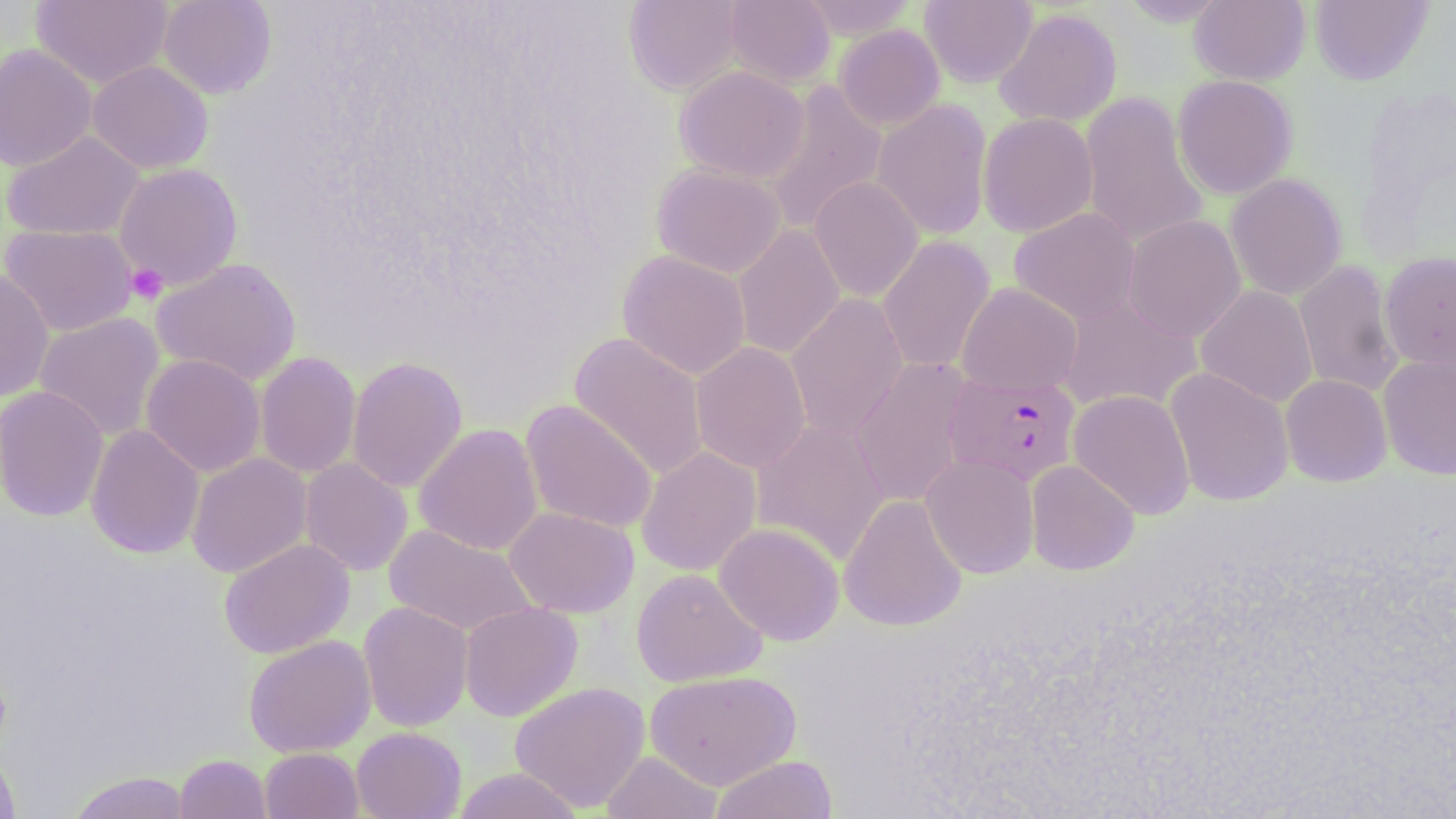

Summary:
  - Coordinate format: approximate bounding boxes as (x1, y1, x2, y2) in pixels
  - Plasmodium falciparum-infected red blood cell locations: (944, 371, 1081, 487)
  - Platelet locations: (126, 263, 168, 305)
  - Uninfected red blood cell locations: (31, 0, 173, 89), (157, 0, 277, 99), (624, 0, 745, 95), (723, 0, 836, 88), (797, 0, 919, 39), (920, 0, 1037, 88), (1119, 0, 1231, 26), (1190, 0, 1310, 85), (1310, 0, 1432, 85), (994, 7, 1122, 128), (833, 24, 945, 131), (0, 43, 98, 171), (87, 60, 213, 174), (674, 65, 810, 183), (1172, 74, 1297, 199), (761, 81, 888, 235), (1079, 92, 1209, 250), (872, 99, 992, 241), (978, 112, 1098, 238), (2, 130, 144, 241), (114, 162, 244, 290), (651, 163, 787, 278), (1226, 173, 1346, 300), (808, 176, 924, 303), (1009, 207, 1140, 324), (1123, 214, 1246, 342), (0, 224, 139, 336), (732, 225, 845, 359), (877, 235, 996, 374), (616, 250, 752, 380), (1379, 251, 1456, 371), (151, 258, 302, 386), (1294, 260, 1404, 398), (0, 268, 54, 401), (956, 283, 1083, 396), (1196, 285, 1318, 408), (786, 292, 909, 442), (1055, 292, 1203, 414), (34, 312, 166, 442), (569, 332, 709, 481), (691, 342, 811, 473), (255, 351, 361, 479), (141, 354, 266, 477), (1378, 354, 1456, 480), (346, 356, 468, 493), (850, 358, 974, 507), (1165, 367, 1294, 507), (1281, 374, 1392, 486), (0, 385, 110, 522), (1069, 389, 1195, 519), (520, 400, 658, 534), (751, 419, 890, 566), (414, 423, 543, 556), (85, 424, 205, 559), (636, 446, 762, 576), (187, 453, 312, 578), (920, 453, 1040, 579), (300, 457, 413, 576), (1026, 460, 1139, 575), (839, 494, 967, 632), (504, 506, 639, 618), (714, 522, 844, 645), (384, 524, 538, 637), (219, 538, 355, 659), (631, 568, 767, 687), (358, 601, 473, 732), (459, 602, 583, 722), (243, 635, 376, 757), (645, 670, 800, 789), (510, 681, 651, 812), (351, 727, 466, 819), (0, 747, 20, 818), (259, 747, 363, 819), (601, 750, 723, 819), (174, 754, 272, 818), (710, 755, 838, 818), (451, 767, 584, 819), (67, 771, 193, 819)
  - Slide-level diagnosis: Plasmodium falciparum
  - Modality: optical microscopy
  - Preparation: thin blood film
  - Stain: May-Grünwald-Giemsa
  - Magnification: 1000x
  - Field of view: single
  - Image size: 1456×819 pixels